Name the parasite shown.
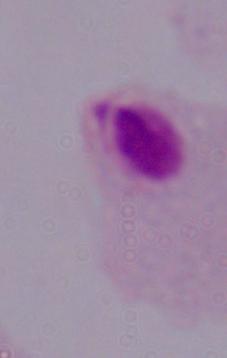

A trichomonad.

modality: photomicrograph
magnification: 1000x